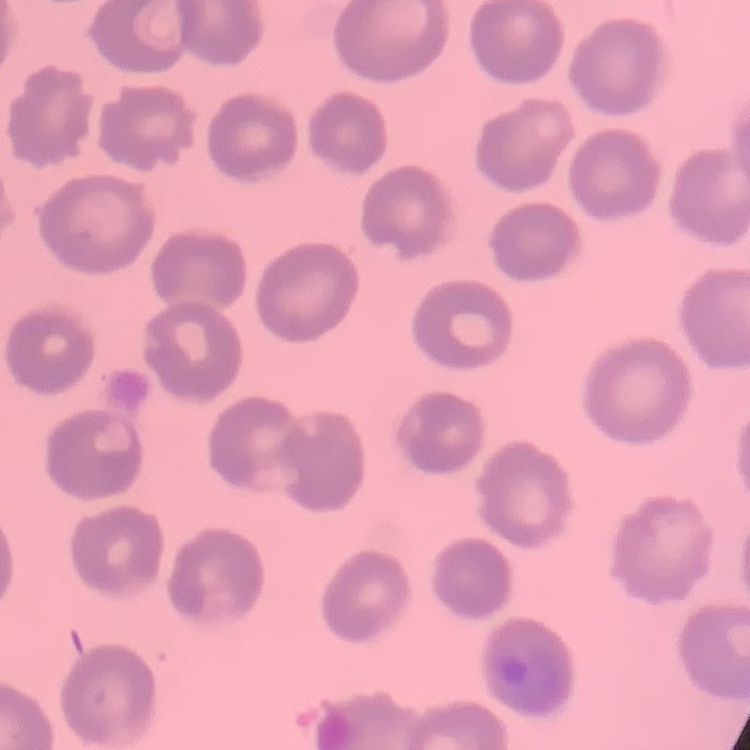 The erythrocytes show no rouleaux formation. Thin blood smear. One tile cut from a larger photomicrograph. Stained with either Field's or Giemsa.